Comment on the morphology of the erythrocytes.
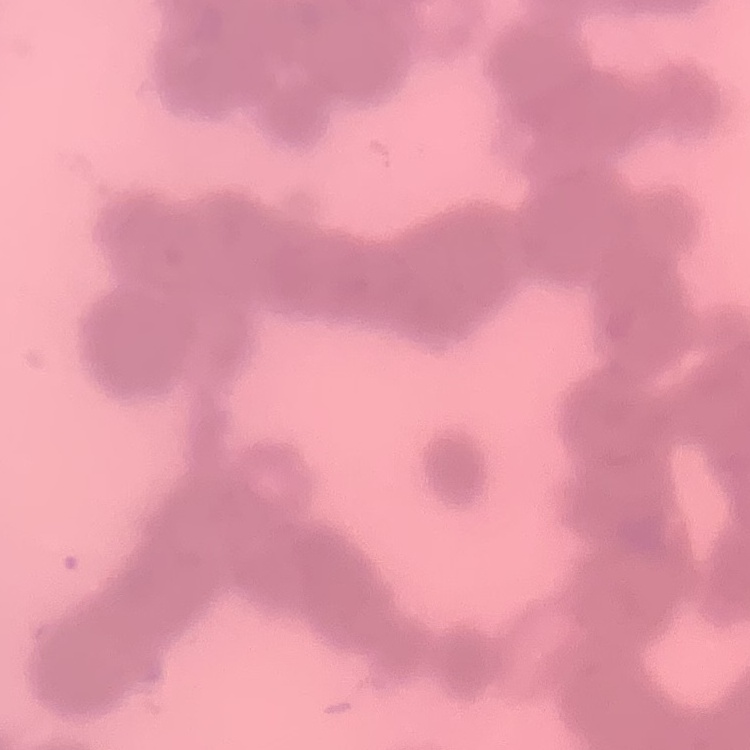

Rouleaux formation.

Summary:
  - Image type: square crop of a larger photomicrograph
  - Stain: Field's or Giemsa
  - Preparation: thin blood smear